Comment on the morphology of the erythrocytes.
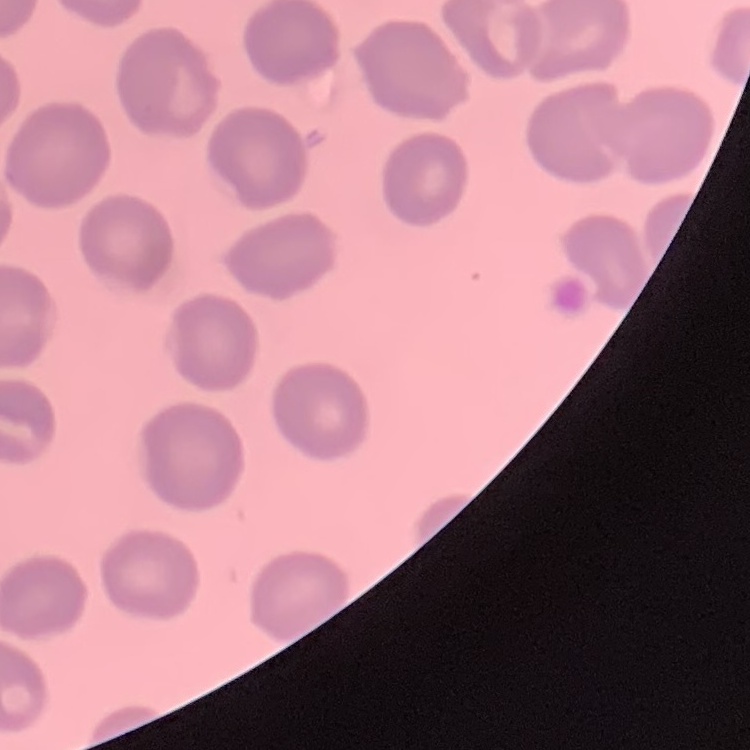
No rouleaux formation.

image type = one tile cut from a larger photomicrograph
preparation = thin peripheral smear
stain = Field's or Giemsa